Give the extent of all uninfected red blood cells.
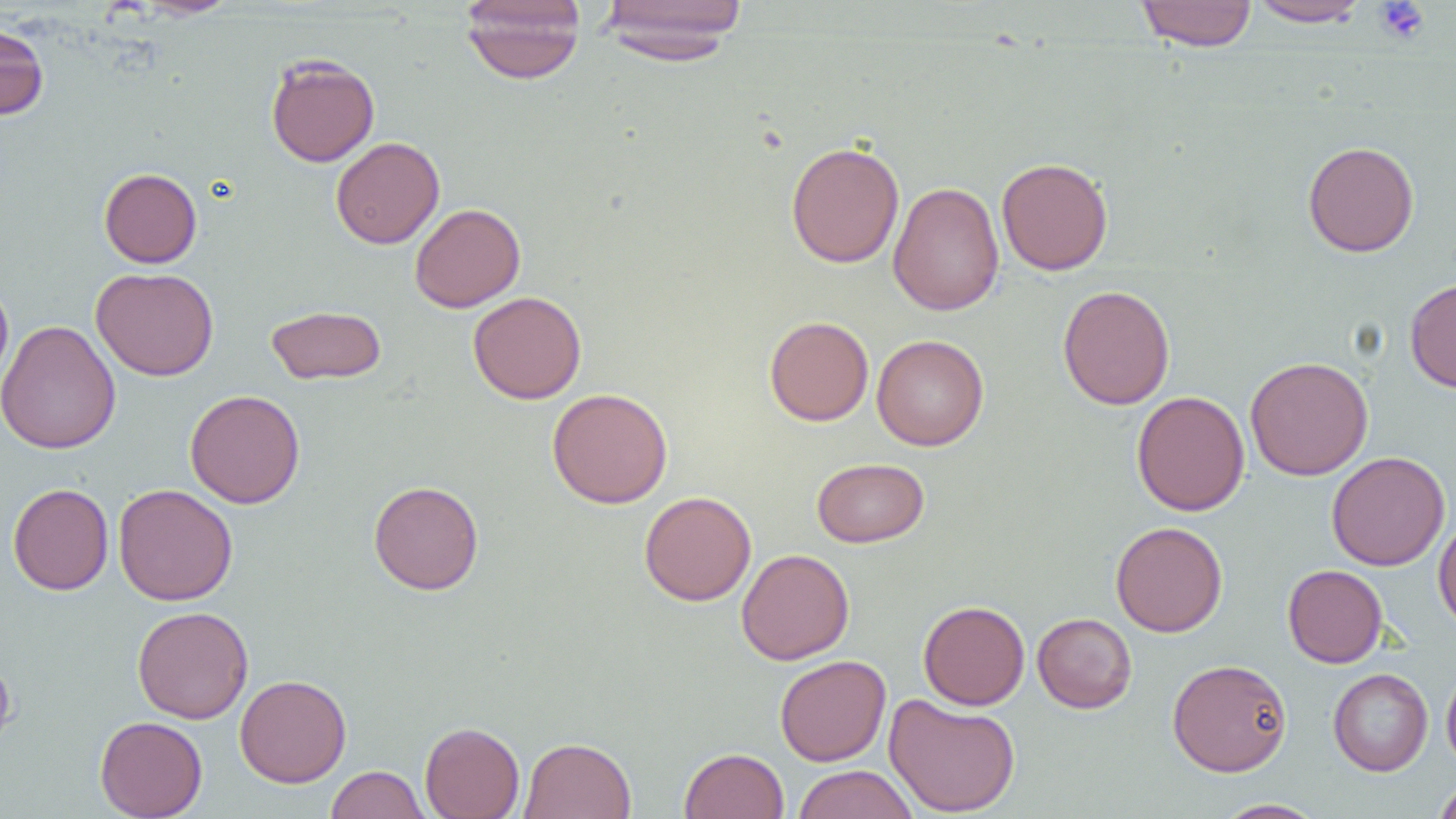

Approximate bounding boxes as [x1, y1, x2, y2] in pixels.
Uninfected red blood cells: [131, 0, 241, 19], [460, 0, 585, 84], [1136, 0, 1257, 51], [596, 1, 749, 63], [1247, 1, 1372, 28], [0, 20, 49, 122], [265, 53, 380, 167], [331, 137, 444, 249], [786, 140, 904, 269], [1303, 140, 1419, 257], [996, 157, 1113, 276], [99, 167, 202, 268], [887, 182, 1005, 315], [409, 203, 526, 312], [90, 267, 219, 381], [1405, 277, 1456, 393], [0, 280, 14, 395], [1058, 284, 1175, 410], [468, 291, 586, 404], [266, 305, 387, 385], [764, 316, 874, 426], [0, 320, 120, 454], [872, 334, 989, 450], [1245, 356, 1374, 480], [547, 388, 673, 508], [185, 389, 305, 508], [1132, 391, 1250, 516], [1326, 451, 1450, 571], [812, 457, 929, 547], [368, 480, 484, 594], [8, 483, 113, 595], [113, 484, 238, 606], [639, 490, 757, 606], [1433, 514, 1456, 634], [1110, 521, 1228, 637], [737, 549, 855, 665], [1283, 564, 1387, 668], [918, 600, 1030, 710], [132, 605, 253, 723], [1032, 613, 1137, 713], [0, 650, 17, 758], [775, 654, 891, 766], [1167, 658, 1292, 776], [1441, 664, 1456, 774], [1328, 669, 1433, 776], [235, 674, 352, 787], [883, 693, 1021, 817], [94, 715, 208, 819], [420, 721, 524, 819], [519, 736, 636, 818], [679, 747, 789, 819], [792, 764, 919, 819], [326, 765, 428, 819], [1433, 778, 1456, 819], [1214, 799, 1326, 818].

Summary:
  - Platelet locations: [1373, 1, 1430, 44]
  - Slide-level diagnosis: no evidence of blood parasites
  - Field of view: one of a larger specimen
  - Modality: optical microscopy
  - Image size: 1456×819 pixels
  - Magnification: 1000x
  - Preparation: thin blood film